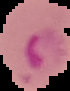
Segmented cell region on a black background. Result: Plasmodium parasites detected. From a thin blood smear. Image is 70×91 pixels.